Report the malaria status of this cell.
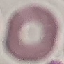

It is uninfected.

Summary:
  - Image type: cell patch, automatically extracted from a larger field of view and resized to 64 × 64 pixels
  - Capture: smartphone camera at the microscope eyepiece
  - Stain: Giemsa
  - Preparation: thin blood smear